Report the malaria status of this cell.
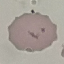
It is uninfected.

stain: Giemsa
preparation: thin smear
image_type: automatically extracted cell patch, resized to 64 × 64 pixels
capture: smartphone camera at the microscope eyepiece